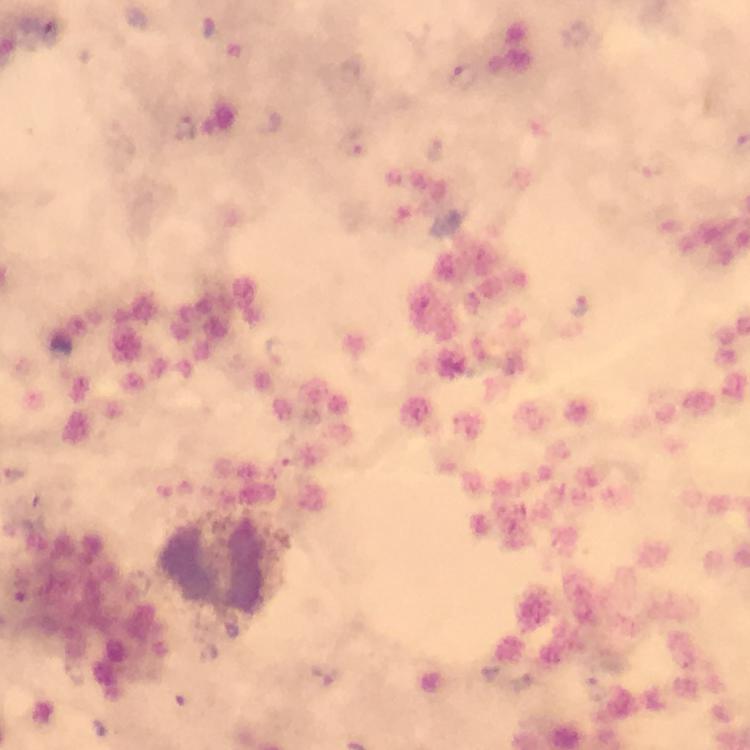 Approximate centers as {x, y} in pixels. Plasmodium parasite locations: {464, 77}, {186, 130}, {357, 143}, {580, 305}, {280, 350}. Smartphone photograph taken through a microscope. Image is 750×750 pixels. Giemsa-stained preparation. At 100x magnification. Thick blood smear. From a diagnostic examination for malaria. Cropped region of a single field of view. Immersion oil applied.